Describe the morphology of the red blood cells.
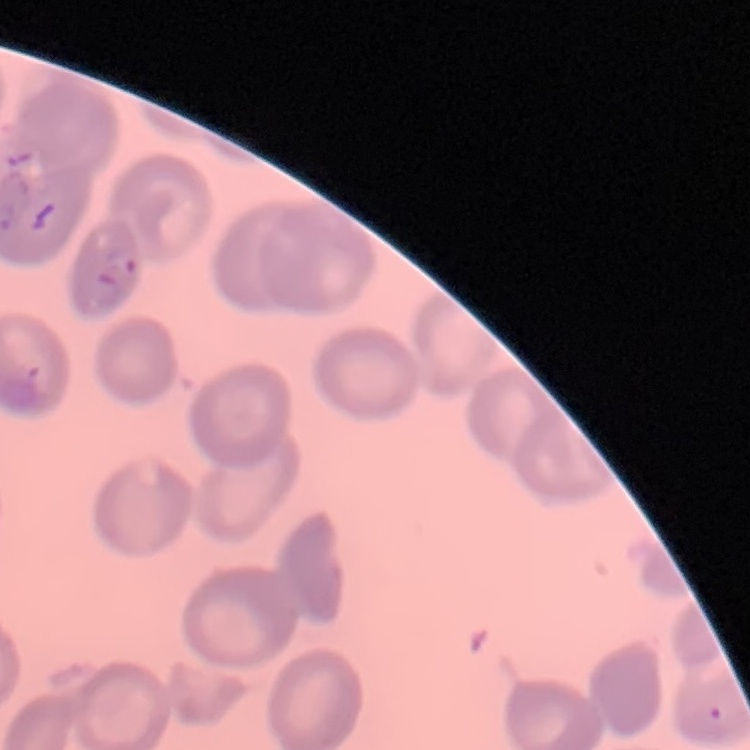
They show no rouleaux formation.

Field's or Giemsa stain. One tile cut from a larger photomicrograph. Thin blood smear.